Outline each Plasmodium falciparum-infected red blood cell.
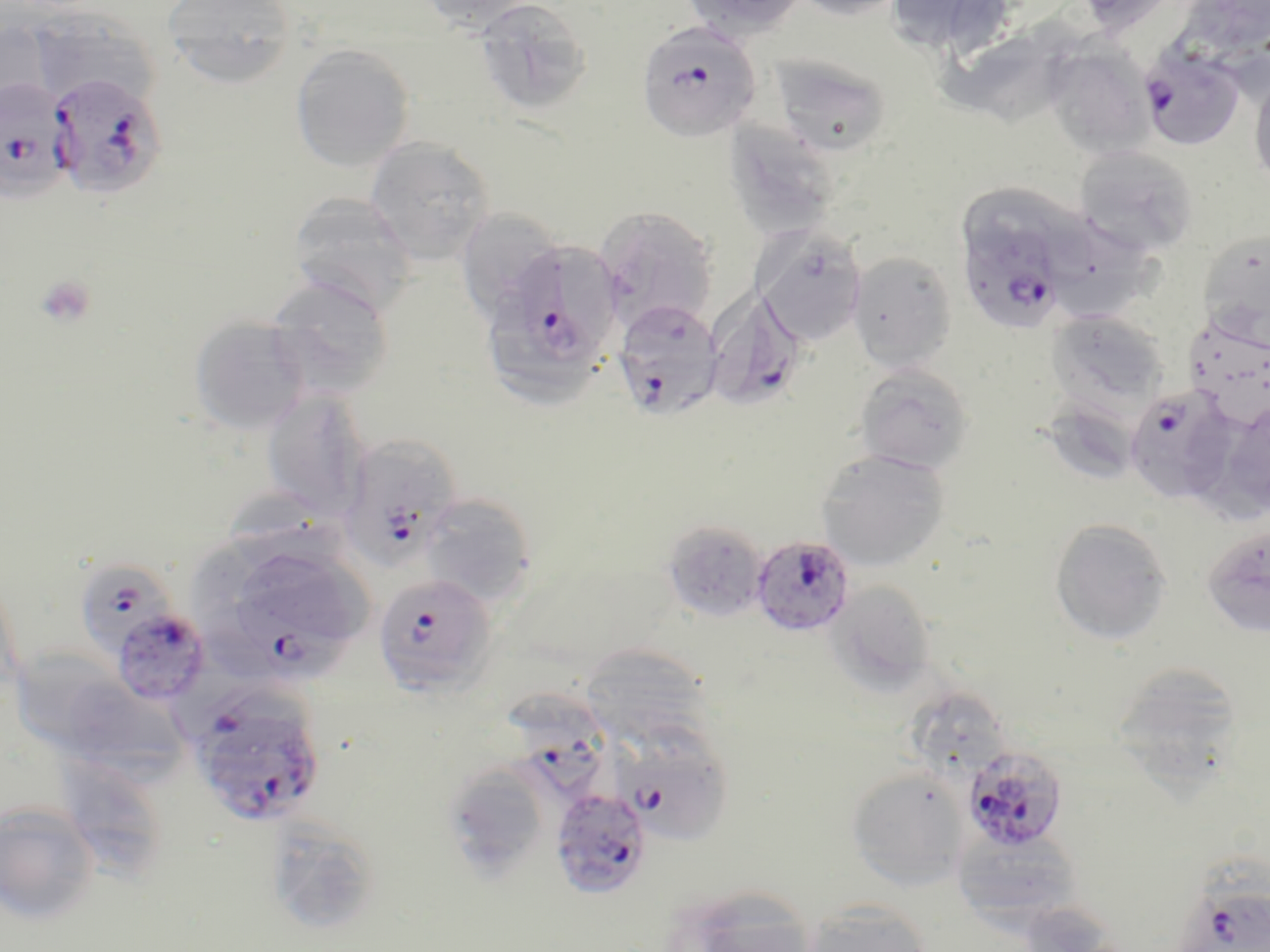
Approximate bounding boxes as (x1, y1, x2, y2) in pixels.
Plasmodium falciparum-infected red blood cells (subset): (636, 19, 763, 143), (1138, 43, 1245, 151), (47, 72, 166, 200), (0, 78, 75, 203), (958, 233, 1069, 327), (520, 244, 619, 363), (708, 285, 806, 410), (613, 300, 726, 420), (1124, 385, 1238, 503), (339, 434, 464, 572), (750, 536, 856, 640), (78, 559, 173, 654), (372, 571, 496, 696), (108, 606, 212, 708), (505, 689, 614, 795), (208, 718, 323, 824), (608, 719, 734, 844), (962, 745, 1069, 852), (550, 786, 652, 900).

Summary:
  - Platelet locations: (34, 274, 98, 329)
  - Uninfected red blood cell locations (subset): (162, 0, 299, 87), (416, 0, 540, 31), (679, 0, 796, 43), (790, 0, 909, 21), (883, 0, 1017, 57), (1072, 0, 1185, 35), (475, 1, 593, 116), (27, 8, 162, 108), (0, 21, 53, 115), (944, 22, 1091, 130), (1043, 41, 1156, 158), (290, 43, 414, 172), (769, 54, 892, 157), (1249, 71, 1270, 190), (723, 120, 842, 242), (364, 137, 496, 264), (1073, 145, 1200, 256), (961, 181, 1102, 282), (287, 192, 418, 315), (594, 205, 719, 332), (461, 210, 566, 321), (1053, 222, 1163, 321), (754, 227, 868, 346), (1199, 227, 1270, 335), (847, 251, 957, 372), (265, 275, 395, 400), (489, 299, 602, 410), (1046, 309, 1169, 413), (188, 315, 310, 434), (1183, 321, 1270, 430), (853, 363, 975, 474), (261, 387, 370, 519), (1040, 397, 1142, 487), (1222, 398, 1270, 517), (815, 450, 950, 571), (227, 486, 342, 565), (418, 492, 538, 606), (1049, 517, 1173, 645), (661, 520, 768, 623), (1200, 522, 1270, 638), (184, 530, 286, 623), (826, 579, 938, 694), (17, 643, 109, 748), (579, 643, 711, 748), (1109, 661, 1249, 785), (68, 672, 182, 783), (909, 688, 1010, 771), (68, 758, 162, 874), (456, 765, 544, 881), (845, 768, 969, 889), (0, 800, 100, 925), (264, 816, 382, 935), (951, 828, 1082, 928), (1182, 880, 1270, 952), (660, 883, 821, 952), (802, 899, 935, 952)
  - Slide-level diagnosis: Plasmodium falciparum
  - Field of view: one of a larger specimen
  - Modality: light microscopy
  - Image size: 1270×952 pixels
  - Magnification: 1000x
  - Preparation: thin blood smear
  - Stain: May-Grünwald-Giemsa